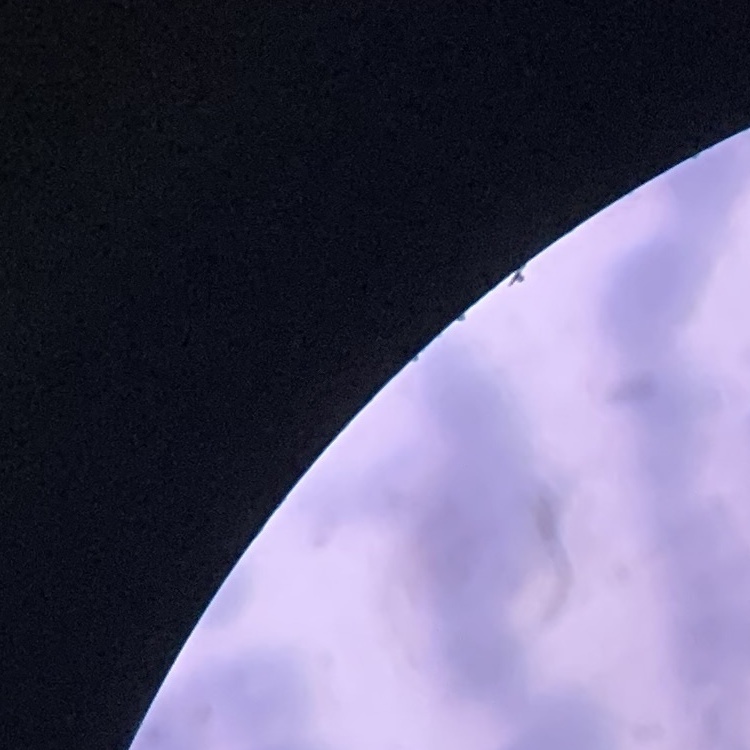

{
  "erythrocyte_morphology": "rouleaux formation",
  "preparation": "thin blood smear",
  "stain": "Field's or Giemsa",
  "image_type": "square crop of a larger photomicrograph"
}